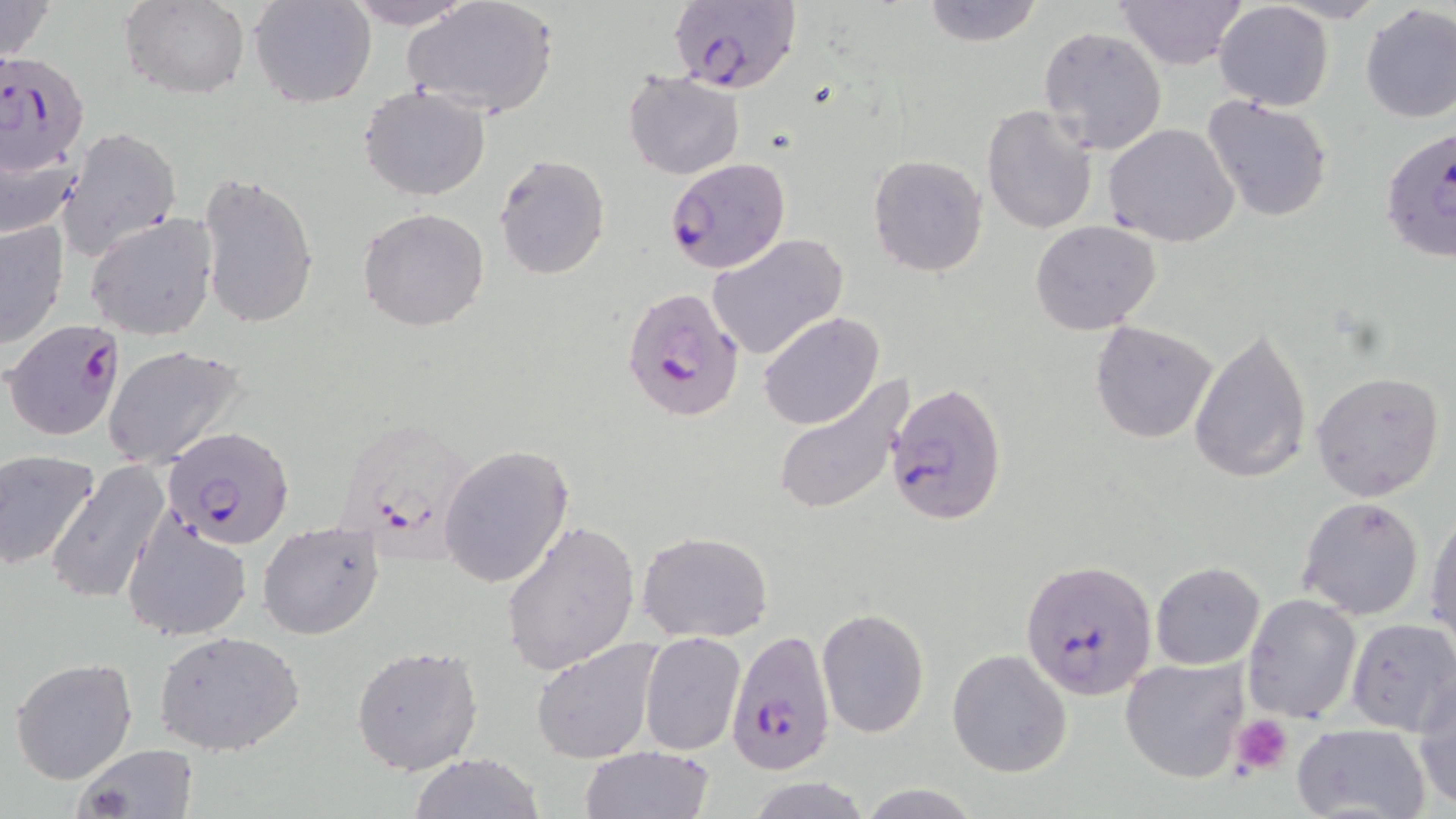
slide-level diagnosis = Plasmodium falciparum
modality = optical microscopy
magnification = 1000x
platelet locations = approximate bounding boxes as named x1/y1/x2/y2 corners in pixels: (x1=1230, y1=714, x2=1293, y2=777)
image size = 1456×819 pixels
stain = May-Grünwald-Giemsa
uninfected red blood cell locations = approximate bounding boxes as named x1/y1/x2/y2 corners in pixels: (x1=0, y1=0, x2=57, y2=64), (x1=119, y1=0, x2=251, y2=101), (x1=250, y1=0, x2=377, y2=107), (x1=344, y1=0, x2=477, y2=28), (x1=401, y1=0, x2=560, y2=120), (x1=921, y1=0, x2=1042, y2=47), (x1=1115, y1=0, x2=1246, y2=70), (x1=1213, y1=3, x2=1334, y2=112), (x1=1358, y1=4, x2=1456, y2=124), (x1=1038, y1=26, x2=1168, y2=155), (x1=623, y1=71, x2=745, y2=180), (x1=357, y1=85, x2=492, y2=201), (x1=1201, y1=94, x2=1333, y2=225), (x1=982, y1=103, x2=1100, y2=235), (x1=1102, y1=122, x2=1241, y2=249), (x1=59, y1=126, x2=182, y2=261), (x1=0, y1=133, x2=85, y2=241), (x1=867, y1=154, x2=990, y2=277), (x1=495, y1=155, x2=611, y2=279), (x1=196, y1=171, x2=321, y2=335), (x1=357, y1=207, x2=491, y2=332), (x1=85, y1=212, x2=219, y2=341), (x1=1, y1=218, x2=70, y2=349), (x1=1029, y1=220, x2=1162, y2=335), (x1=706, y1=233, x2=848, y2=361), (x1=758, y1=311, x2=884, y2=430), (x1=1090, y1=320, x2=1218, y2=443), (x1=1187, y1=325, x2=1311, y2=484), (x1=102, y1=343, x2=249, y2=469), (x1=1310, y1=371, x2=1445, y2=503), (x1=770, y1=375, x2=913, y2=518), (x1=438, y1=445, x2=574, y2=589), (x1=0, y1=451, x2=101, y2=572), (x1=44, y1=460, x2=171, y2=606), (x1=1296, y1=496, x2=1425, y2=620), (x1=1426, y1=499, x2=1456, y2=646), (x1=121, y1=513, x2=253, y2=642), (x1=256, y1=519, x2=387, y2=640), (x1=500, y1=520, x2=641, y2=677), (x1=637, y1=532, x2=773, y2=643), (x1=1151, y1=562, x2=1265, y2=670), (x1=1242, y1=593, x2=1360, y2=723), (x1=816, y1=607, x2=929, y2=738), (x1=1347, y1=616, x2=1455, y2=732), (x1=153, y1=630, x2=306, y2=756), (x1=641, y1=631, x2=747, y2=757), (x1=530, y1=637, x2=664, y2=764), (x1=352, y1=645, x2=483, y2=778), (x1=947, y1=649, x2=1072, y2=777), (x1=9, y1=657, x2=139, y2=784), (x1=1120, y1=658, x2=1251, y2=784), (x1=1412, y1=676, x2=1456, y2=812), (x1=1290, y1=724, x2=1431, y2=819), (x1=70, y1=743, x2=198, y2=818), (x1=579, y1=745, x2=715, y2=819), (x1=407, y1=753, x2=546, y2=819), (x1=746, y1=776, x2=871, y2=818), (x1=856, y1=784, x2=983, y2=818)
preparation = thin blood smear
field of view = single
Plasmodium falciparum-infected red blood cell locations = approximate bounding boxes as named x1/y1/x2/y2 corners in pixels: (x1=673, y1=0, x2=801, y2=94), (x1=4, y1=49, x2=96, y2=173), (x1=1380, y1=124, x2=1455, y2=265), (x1=663, y1=155, x2=790, y2=276), (x1=622, y1=287, x2=748, y2=424), (x1=5, y1=320, x2=129, y2=442), (x1=885, y1=382, x2=1009, y2=527), (x1=336, y1=421, x2=484, y2=568), (x1=165, y1=429, x2=293, y2=549), (x1=1021, y1=560, x2=1157, y2=697), (x1=727, y1=629, x2=834, y2=775)